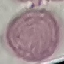

malaria status = uninfected
preparation = thin blood film
stain = Giemsa
image type = automatically extracted cell patch, resized to 64 × 64 pixels
capture = smartphone camera at the microscope eyepiece